Report the malaria status of this cell.
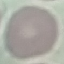
Uninfected.

Summary:
  - Preparation: thin smear
  - Stain: Giemsa
  - Capture: smartphone through the microscope eyepiece
  - Image type: automatically extracted cell patch, resized to 64 × 64 pixels